Report the malaria status of this cell.
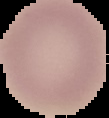

Uninfected.

preparation: thin blood film
image_size: 109×118 pixels
image_type: segmented cell region on a black background